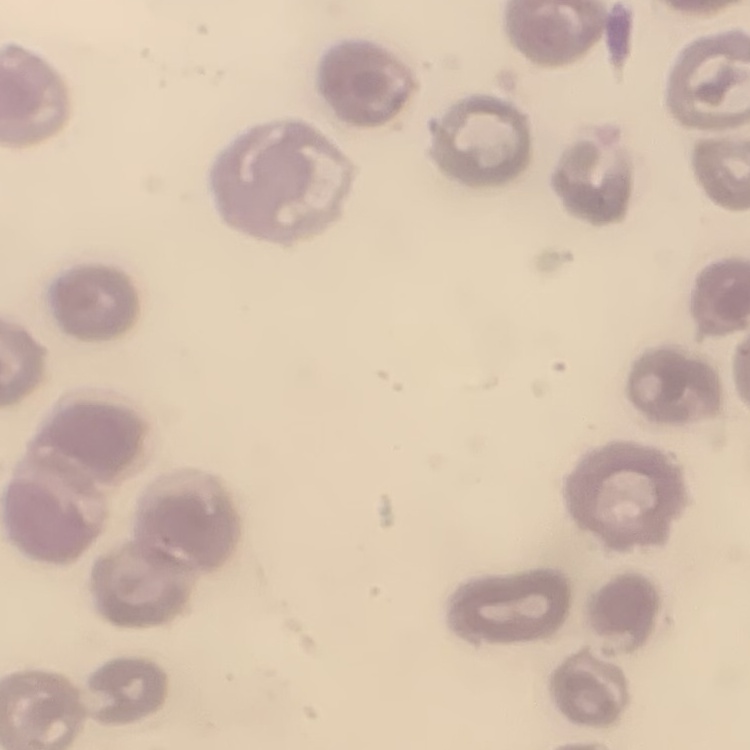

erythrocyte morphology = no rouleaux formation
preparation = thin blood smear
stain = Field's or Giemsa
image type = square crop of a larger photomicrograph